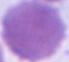
Summary:
  - Identification: erythrocyte
  - Modality: photomicrograph
  - Magnification: 1000x